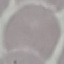 Malaria status: uninfected. Cell patch, automatically extracted from a larger field of view and resized to 64 × 64 pixels. Giemsa-stained preparation. Thin blood film. Acquired by smartphone through the microscope eyepiece.